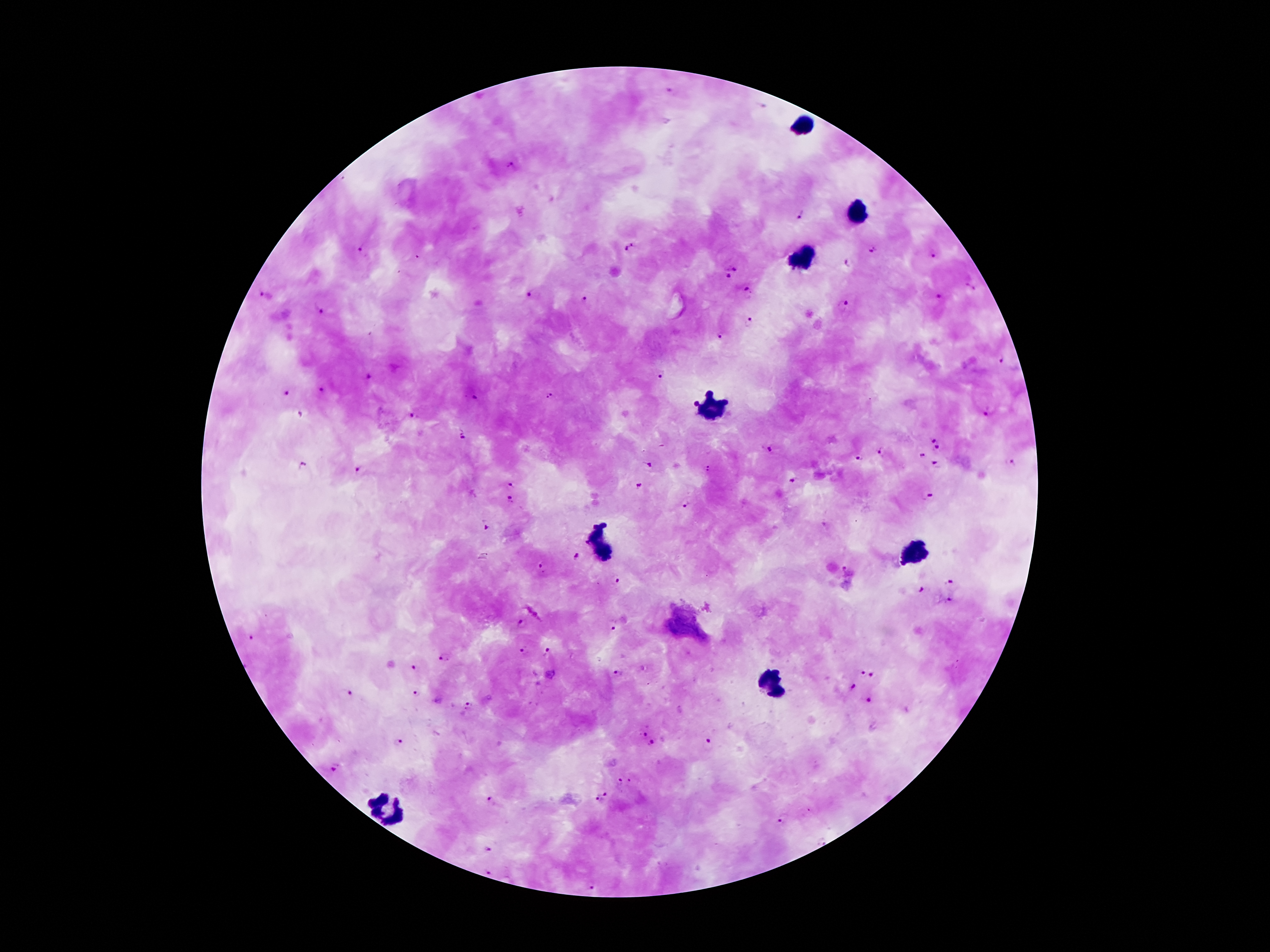
coordinate format = approximate centers as [x, y] in pixels
leukocyte locations = [803, 124], [858, 210], [803, 256], [712, 408], [597, 539], [914, 551], [774, 682], [388, 812]
malaria parasite locations = [671, 91], [765, 105], [511, 166], [801, 215], [624, 245], [360, 251], [875, 251], [933, 255], [849, 262], [734, 268], [728, 276], [970, 288], [748, 290], [531, 295], [937, 295], [263, 296], [584, 300], [843, 303], [324, 310], [749, 323], [720, 335], [1001, 360], [368, 374], [661, 374], [322, 391], [285, 394], [550, 397], [475, 398], [984, 412], [301, 413], [411, 414], [462, 435], [934, 439], [935, 447], [771, 449], [883, 453], [923, 455], [858, 460], [650, 463], [1011, 464], [303, 465], [935, 465], [359, 469], [709, 471], [793, 482], [512, 484], [639, 487], [927, 497], [510, 499], [687, 503], [484, 527], [576, 557], [543, 567], [841, 570], [952, 580], [617, 581], [919, 590], [951, 599], [518, 625], [612, 627], [250, 637], [522, 653], [547, 653], [447, 658], [413, 668], [862, 671], [617, 672], [873, 675], [852, 687], [350, 694], [417, 694], [868, 699], [469, 706], [643, 732], [399, 741], [710, 741], [650, 742], [333, 769], [619, 781], [606, 794], [597, 799], [490, 800], [782, 820], [822, 842], [487, 850], [489, 874], [594, 887]
preparation = thick blood smear
capture = smartphone through the microscope eyepiece
magnification = 100x
image size = 1270×952 pixels
field of view = one from this slide
stain = Giemsa
patient malaria status = positive for Plasmodium falciparum